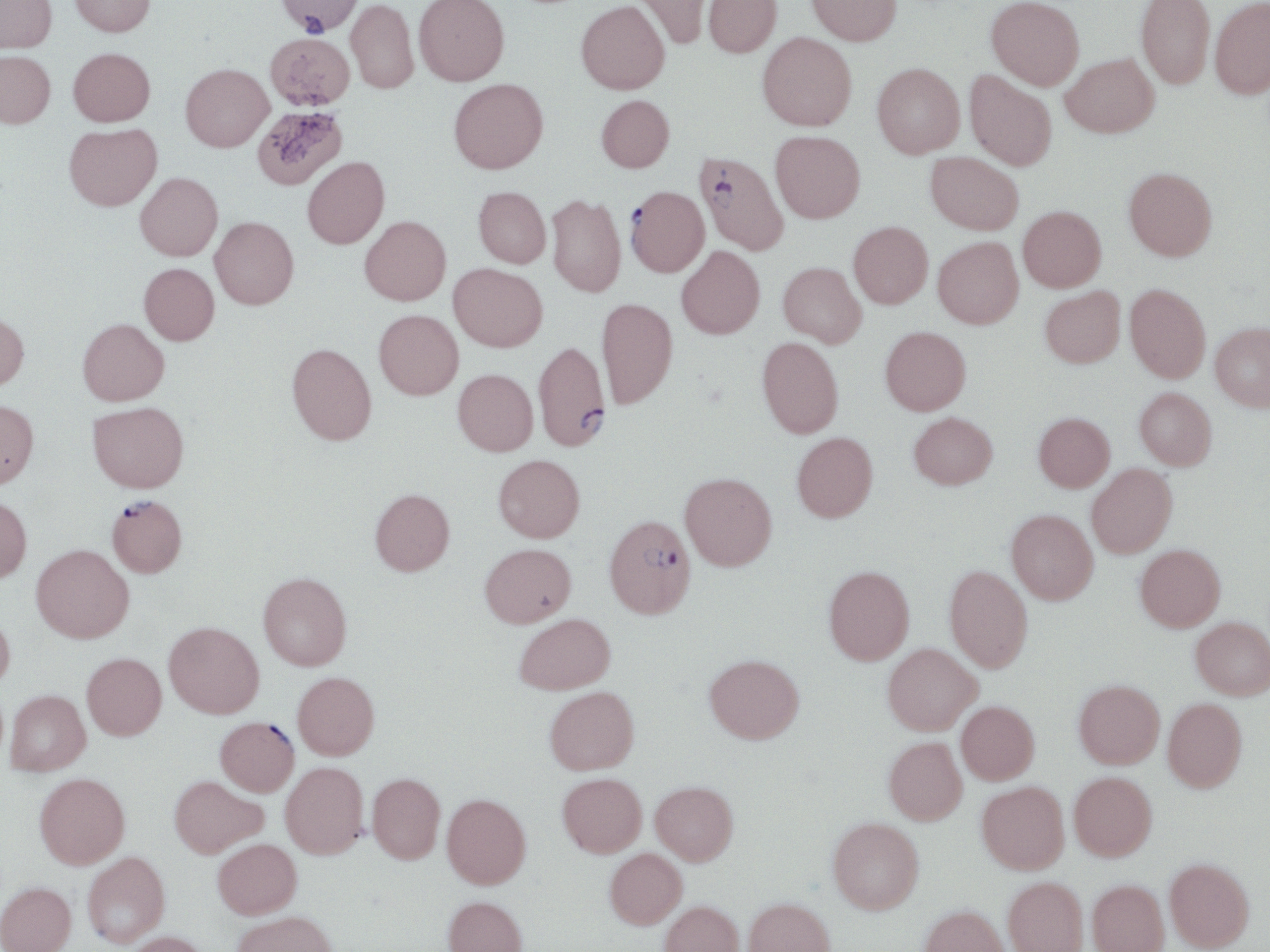
Summary:
  - Coordinate format: approximate bounding boxes as (x1, y1, x2, y2) in pixels
  - Uninfected red blood cell locations: (0, 0, 56, 53), (70, 0, 156, 37), (276, 0, 364, 36), (413, 0, 509, 86), (634, 0, 714, 49), (703, 0, 782, 57), (806, 0, 902, 45), (1135, 0, 1215, 90), (1210, 0, 1270, 99), (345, 1, 419, 94), (576, 1, 669, 94), (986, 1, 1085, 90), (265, 32, 355, 110), (757, 32, 856, 131), (68, 47, 155, 126), (0, 50, 55, 128), (1060, 53, 1159, 137), (872, 63, 965, 158), (181, 64, 273, 152), (965, 71, 1057, 171), (448, 78, 548, 174), (596, 94, 674, 172), (251, 104, 349, 191), (64, 123, 162, 211), (770, 130, 865, 223), (926, 152, 1024, 234), (302, 157, 389, 249), (1124, 167, 1217, 261), (135, 172, 222, 260), (473, 186, 551, 268), (547, 193, 626, 298), (1018, 206, 1106, 292), (210, 216, 298, 309), (359, 216, 451, 305), (848, 221, 933, 308), (933, 237, 1023, 329), (676, 246, 765, 339), (779, 261, 866, 347), (139, 263, 219, 345), (449, 263, 547, 351), (1125, 283, 1211, 383), (1040, 286, 1125, 367), (596, 297, 677, 409), (374, 310, 463, 399), (0, 312, 29, 392), (78, 318, 169, 406), (1210, 321, 1270, 411), (880, 326, 971, 415), (757, 337, 843, 438), (287, 343, 377, 445), (453, 369, 538, 456), (1134, 387, 1217, 470), (0, 399, 39, 489), (88, 402, 188, 492), (909, 412, 998, 489), (1033, 412, 1115, 492), (792, 432, 878, 522), (494, 454, 585, 542), (1087, 463, 1177, 558), (680, 472, 777, 570), (370, 488, 454, 575), (0, 494, 32, 582), (1006, 509, 1098, 604), (480, 543, 577, 627), (31, 544, 134, 642), (1135, 544, 1226, 631), (944, 564, 1033, 672), (823, 565, 915, 664), (258, 572, 352, 670), (0, 612, 15, 689), (514, 613, 615, 695), (1191, 616, 1270, 700), (164, 621, 264, 718), (883, 643, 981, 734), (82, 653, 166, 740), (704, 654, 804, 744), (293, 672, 379, 759), (1073, 679, 1165, 769), (545, 686, 639, 774), (5, 689, 90, 775), (1163, 698, 1247, 791), (957, 701, 1039, 784), (883, 737, 967, 824), (281, 762, 368, 858), (1069, 771, 1157, 860), (34, 772, 130, 869), (368, 773, 445, 863), (558, 773, 647, 857), (169, 775, 266, 858), (651, 781, 738, 865), (977, 781, 1069, 874), (442, 793, 531, 888), (828, 817, 924, 913), (213, 838, 301, 918), (605, 848, 686, 928), (83, 851, 170, 947), (1164, 858, 1254, 951), (1003, 876, 1088, 952), (1087, 879, 1169, 952), (0, 882, 76, 952), (442, 895, 528, 952), (743, 897, 836, 952), (660, 900, 744, 952), (918, 904, 1012, 952), (232, 910, 339, 952), (123, 931, 211, 952)
  - Plasmodium falciparum-infected red blood cell locations: (693, 154, 794, 261), (625, 186, 710, 277), (533, 341, 610, 451), (106, 494, 187, 577), (604, 515, 696, 618), (215, 716, 299, 796)
  - Slide-level diagnosis: Plasmodium falciparum
  - Preparation: thin blood film
  - Magnification: 1000x
  - Image size: 1270×952 pixels
  - Stain: May-Grünwald-Giemsa
  - Field of view: single
  - Modality: optical microscopy